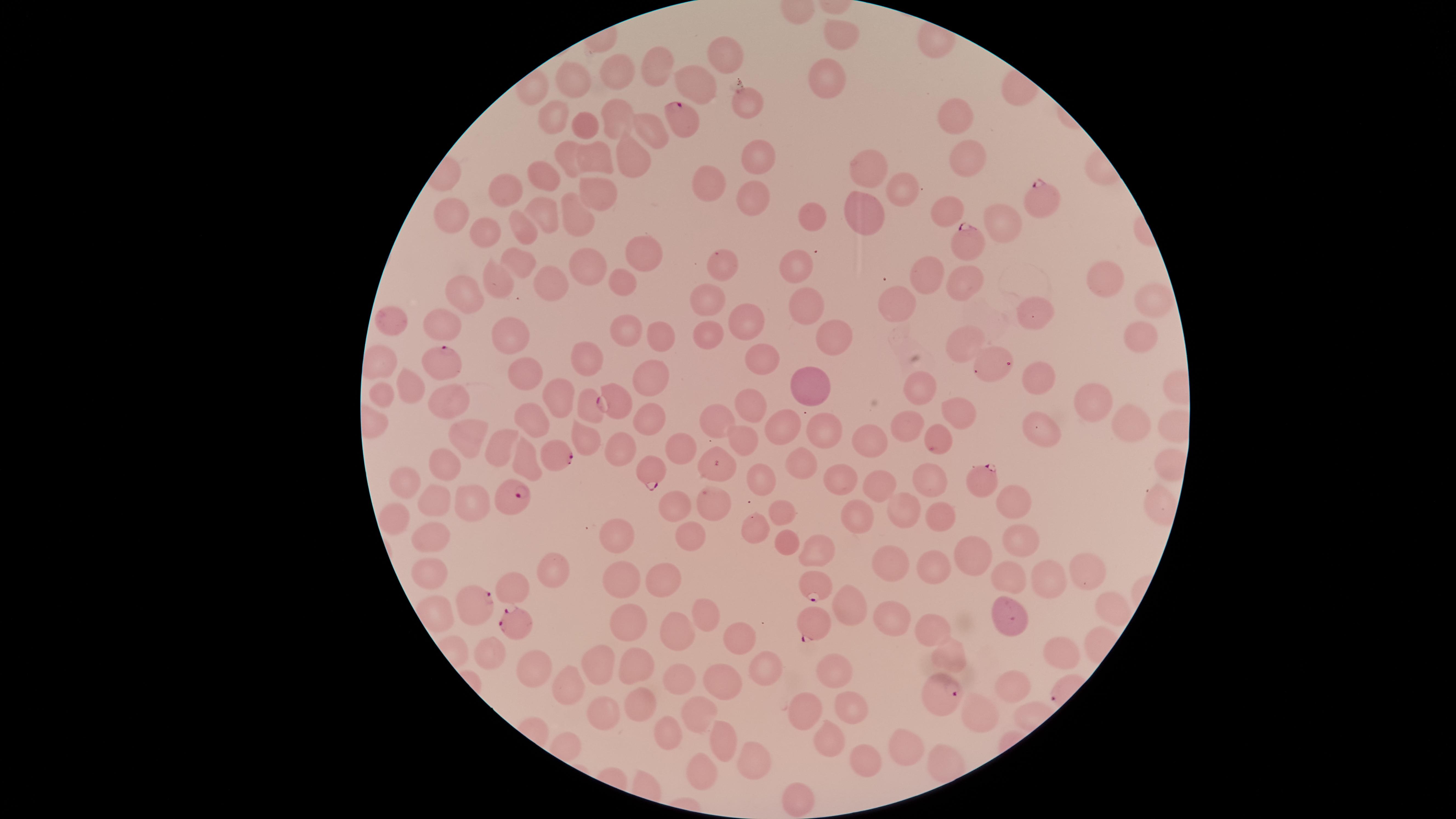 Approximate marker points as {x, y} in pixels. Uninfected red blood cells: {837, 33}, {725, 53}, {658, 66}, {622, 73}, {821, 74}, {577, 76}, {694, 78}, {745, 108}, {550, 111}, {617, 115}, {952, 115}, {585, 123}, {648, 127}, {566, 154}, {593, 154}, {758, 154}, {629, 158}, {968, 159}, {542, 169}, {866, 169}, {709, 181}, {512, 184}, {596, 190}, {902, 190}, {749, 197}, {543, 206}, {945, 209}, {573, 212}, {449, 213}, {863, 213}, {818, 217}, {999, 225}, {523, 227}, {483, 232}, {638, 257}, {795, 262}, {517, 263}, {719, 264}, {586, 269}, {923, 271}, {548, 279}, {621, 281}, {493, 283}, {1110, 283}, {966, 286}, {462, 293}, {896, 295}, {1158, 297}, {705, 299}, {800, 302}, {1031, 316}, {747, 319}, {443, 321}, {391, 324}, {625, 329}, {708, 329}, {1137, 331}, {508, 333}, {822, 337}, {966, 339}, {655, 340}, {586, 354}, {757, 358}, {524, 369}, {1039, 375}, {650, 376}, {812, 384}, {919, 384}, {410, 385}, {380, 391}, {444, 391}, {559, 393}, {1097, 395}, {749, 403}, {587, 404}, {954, 413}, {1130, 413}, {531, 417}, {718, 419}, {649, 420}, {783, 421}, {910, 422}, {825, 426}, {1034, 427}, {586, 434}, {467, 438}, {683, 439}, {744, 439}, {867, 443}, {500, 445}, {619, 450}, {523, 460}, {716, 462}, {800, 462}, {445, 467}, {761, 478}, {840, 479}, {928, 479}, {404, 481}, {876, 484}, {434, 496}, {1017, 499}, {470, 500}, {711, 500}, {671, 508}, {777, 509}, {906, 509}, {392, 513}, {855, 514}, {941, 514}, {619, 532}, {754, 533}, {429, 534}, {1021, 538}, {685, 539}, {786, 545}, {975, 549}, {813, 552}, {892, 565}, {1082, 566}, {553, 569}, {934, 569}, {425, 571}, {1009, 575}, {619, 578}, {515, 581}, {1042, 583}, {664, 584}, {847, 600}, {1105, 606}, {432, 610}, {708, 614}, {1016, 614}, {891, 615}, {630, 619}, {930, 628}, {735, 637}, {675, 638}, {1060, 647}, {486, 650}, {951, 653}, {834, 667}, {600, 668}, {763, 668}, {528, 672}, {636, 672}, {568, 679}, {677, 683}, {1008, 684}, {723, 687}, {637, 704}, {851, 706}, {805, 707}, {600, 710}, {981, 712}, {696, 715}, {667, 736}, {723, 737}, {828, 737}, {905, 748}, {752, 759}, {868, 762}, {699, 773}, {799, 797}. Parasitized red blood cells: {680, 113}, {1040, 200}, {965, 244}, {1007, 365}, {443, 367}, {615, 403}, {939, 441}, {562, 457}, {652, 466}, {980, 476}, {516, 494}, {815, 586}, {476, 606}, {513, 622}, {812, 624}, {944, 699}. Circular visible region. Giemsa-stained preparation. Thin blood smear. Presence: malaria parasites detected. Image is 1456×819 pixels. Photographed with a smartphone camera through the microscope eyepiece. One field of view of the specimen. Species: Plasmodium falciparum.